Classify this cell by malaria status.
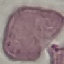

Uninfected.

preparation = thin blood smear
image type = automatically extracted cell patch, resized to 64 × 64 pixels
stain = Giemsa
capture = smartphone through the microscope eyepiece